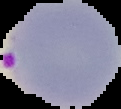
Summary:
  - Image type: cell region segmented out of the field of view; surrounding area masked to black
  - Image size: 121×109 pixels
  - Result: malaria parasites identified
  - Preparation: thin blood film